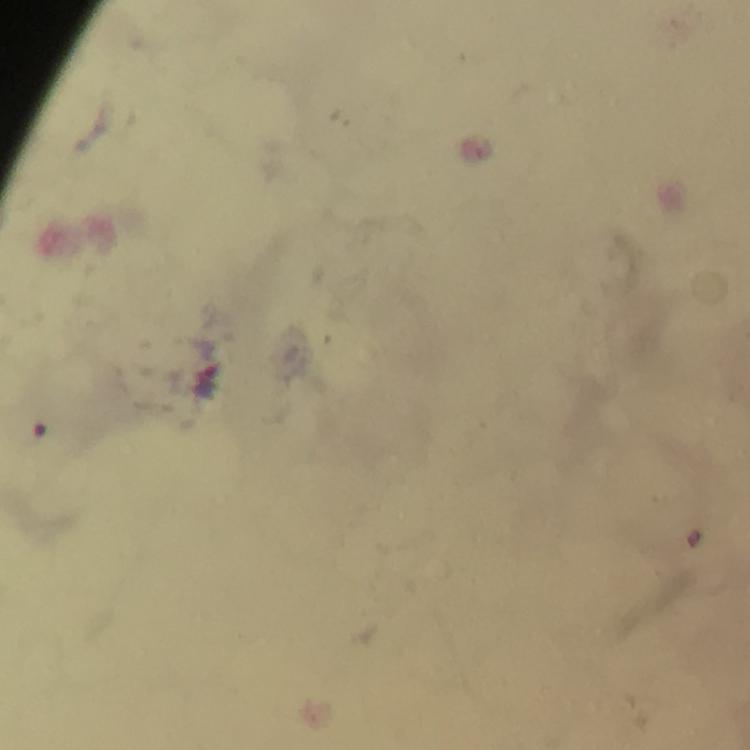

Approximate object centers, in pixels from the top-left corner. Plasmodium parasite locations: (x=207, y=379). 100x magnification. Image is 750×750 pixels. A crop from one field of view. Thick blood film. Immersion oil applied. From a malaria diagnostic workup. Giemsa stain. Smartphone photograph taken through a microscope.